Outline each blood parasite and name the species.
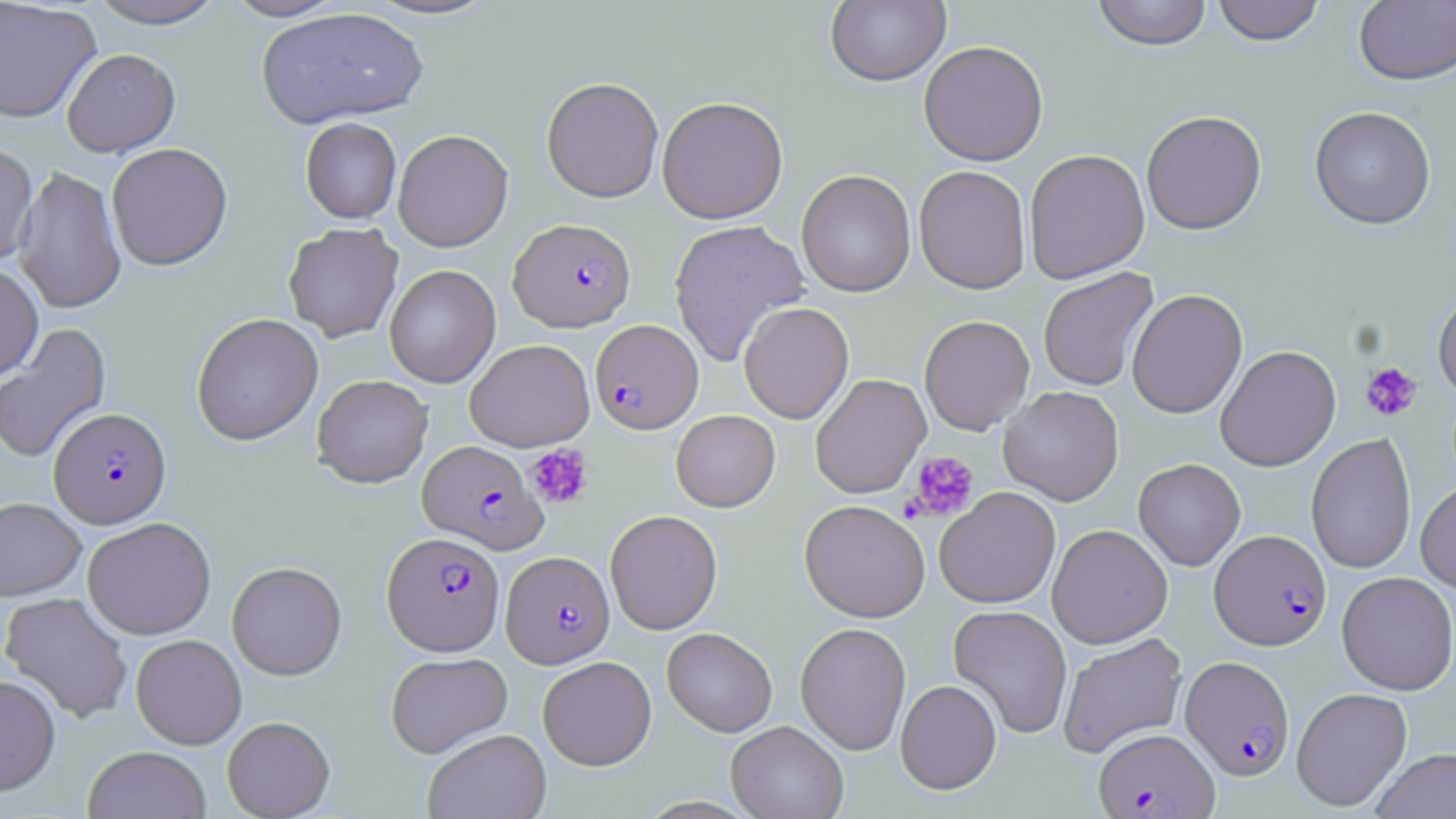
Approximate bounding boxes as [x1, y1, x2, y2] in pixels.
Plasmodium falciparum-infected red blood cells: [509, 218, 636, 331], [590, 319, 703, 434], [49, 407, 171, 528], [417, 440, 548, 554], [1209, 529, 1331, 650], [383, 532, 505, 655], [502, 550, 614, 668], [1180, 656, 1295, 779], [1094, 728, 1219, 818].
No Plasmodium ovale, Plasmodium malariae, Plasmodium vivax, Babesia divergens, or Trypanosoma brucei observed.

Summary:
  - Platelet locations: [1360, 361, 1422, 421], [525, 444, 594, 509], [904, 451, 979, 522]
  - Uninfected red blood cell locations: [85, 0, 228, 29], [219, 0, 351, 21], [360, 0, 502, 21], [825, 0, 950, 86], [1091, 0, 1213, 51], [1211, 0, 1326, 46], [1354, 1, 1456, 86], [0, 2, 102, 124], [255, 7, 428, 129], [918, 40, 1048, 166], [61, 48, 181, 158], [542, 76, 664, 203], [657, 96, 788, 224], [1309, 105, 1436, 229], [1141, 110, 1267, 235], [300, 117, 402, 223], [393, 129, 513, 252], [0, 142, 38, 267], [106, 143, 233, 271], [1024, 149, 1150, 284], [13, 164, 126, 316], [914, 164, 1031, 294], [796, 170, 916, 297], [668, 219, 810, 367], [283, 223, 403, 342], [0, 262, 44, 382], [384, 264, 501, 388], [1037, 268, 1159, 392], [1126, 289, 1248, 419], [1432, 289, 1456, 400], [738, 301, 854, 424], [191, 313, 324, 445], [918, 315, 1035, 435], [0, 323, 112, 465], [465, 339, 594, 451], [1215, 345, 1341, 471], [810, 373, 931, 499], [312, 374, 433, 487], [998, 386, 1124, 506], [671, 410, 780, 512], [1306, 433, 1417, 575], [1133, 458, 1246, 571], [1415, 480, 1456, 593], [934, 487, 1061, 608], [0, 497, 86, 600], [799, 499, 930, 623], [605, 509, 723, 635], [82, 517, 217, 640], [1047, 524, 1173, 649], [227, 561, 347, 680], [1336, 571, 1456, 695], [0, 591, 134, 723], [948, 604, 1073, 739], [795, 622, 911, 755], [662, 627, 777, 737], [1057, 633, 1188, 759], [131, 634, 247, 749], [385, 652, 513, 757], [537, 656, 656, 770], [0, 674, 61, 796], [895, 679, 1002, 794], [1291, 687, 1413, 811], [222, 716, 335, 818], [726, 720, 849, 819], [423, 729, 551, 819], [82, 745, 212, 819], [1370, 748, 1456, 819]
  - Slide-level diagnosis: Plasmodium falciparum
  - Field of view: one of a larger specimen
  - Magnification: 1000x
  - Modality: optical microscopy
  - Preparation: thin blood film
  - Stain: May-Grünwald-Giemsa
  - Image size: 1456×819 pixels